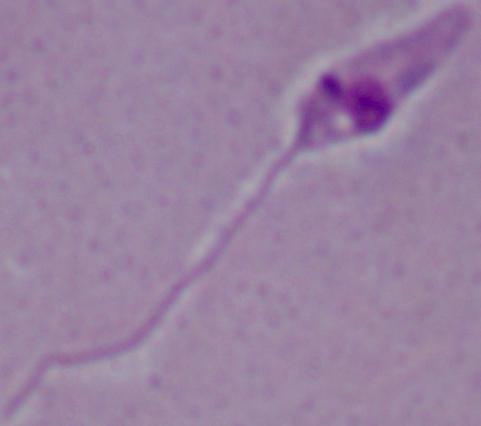
magnification = 1000x
modality = photomicrograph
identification = Leishmania